Assess the morphology of the erythrocytes.
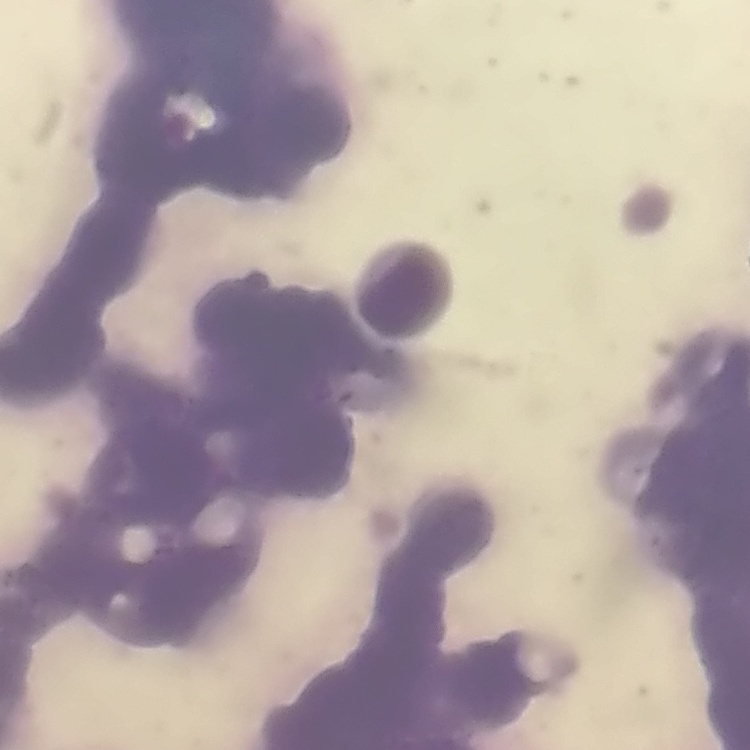

Rouleaux formation.

preparation = thin blood film
stain = Field's or Giemsa
image type = one tile cut from a larger photomicrograph